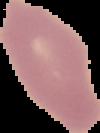
image_type: cell region segmented out of the field of view; surrounding area masked to black
preparation: thin blood film
result: no Plasmodium parasites detected
image_size: 100×133 pixels